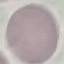
Summary:
  - Malaria status: uninfected
  - Preparation: thin smear
  - Image type: cell patch, automatically extracted from a larger field of view and resized to 64 × 64 pixels
  - Stain: Giemsa
  - Capture: smartphone through the microscope eyepiece